Locate malaria parasites and identify their life-cycle stages.
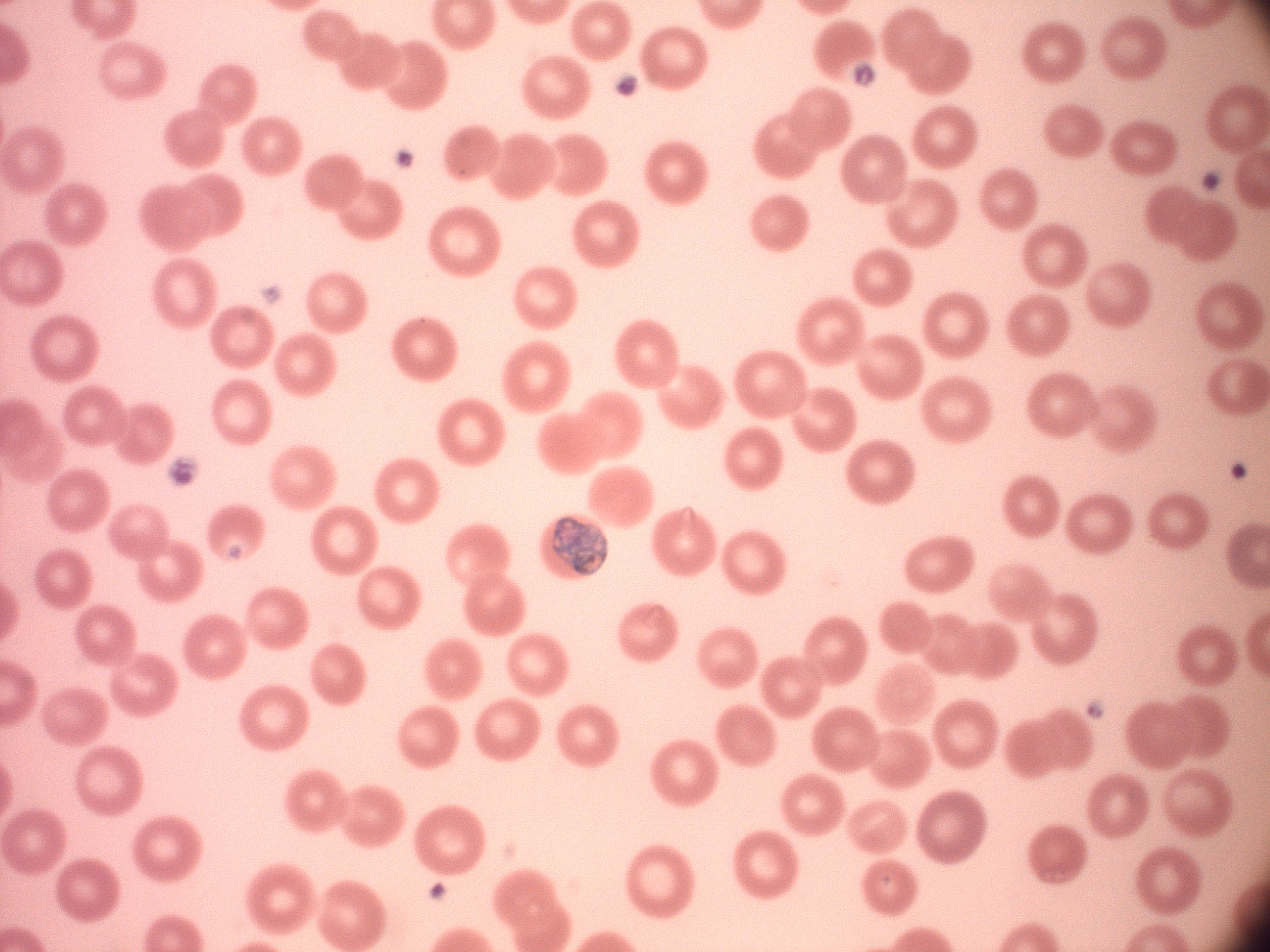

Approximate bounding boxes as named x1/y1/x2/y2 corners in pixels, from the source annotation, which is not necessarily exhaustive.
Schizonts: (x1=551, y1=515, x2=608, y2=576).

microscope = Leica DM2000 with built-in camera
stain = Giemsa
preparation = thin blood film
field of view = one from this slide
magnification = 100x
image size = 1270×952 pixels
species = Plasmodium malariae